Give the position of every Plasmodium parasite.
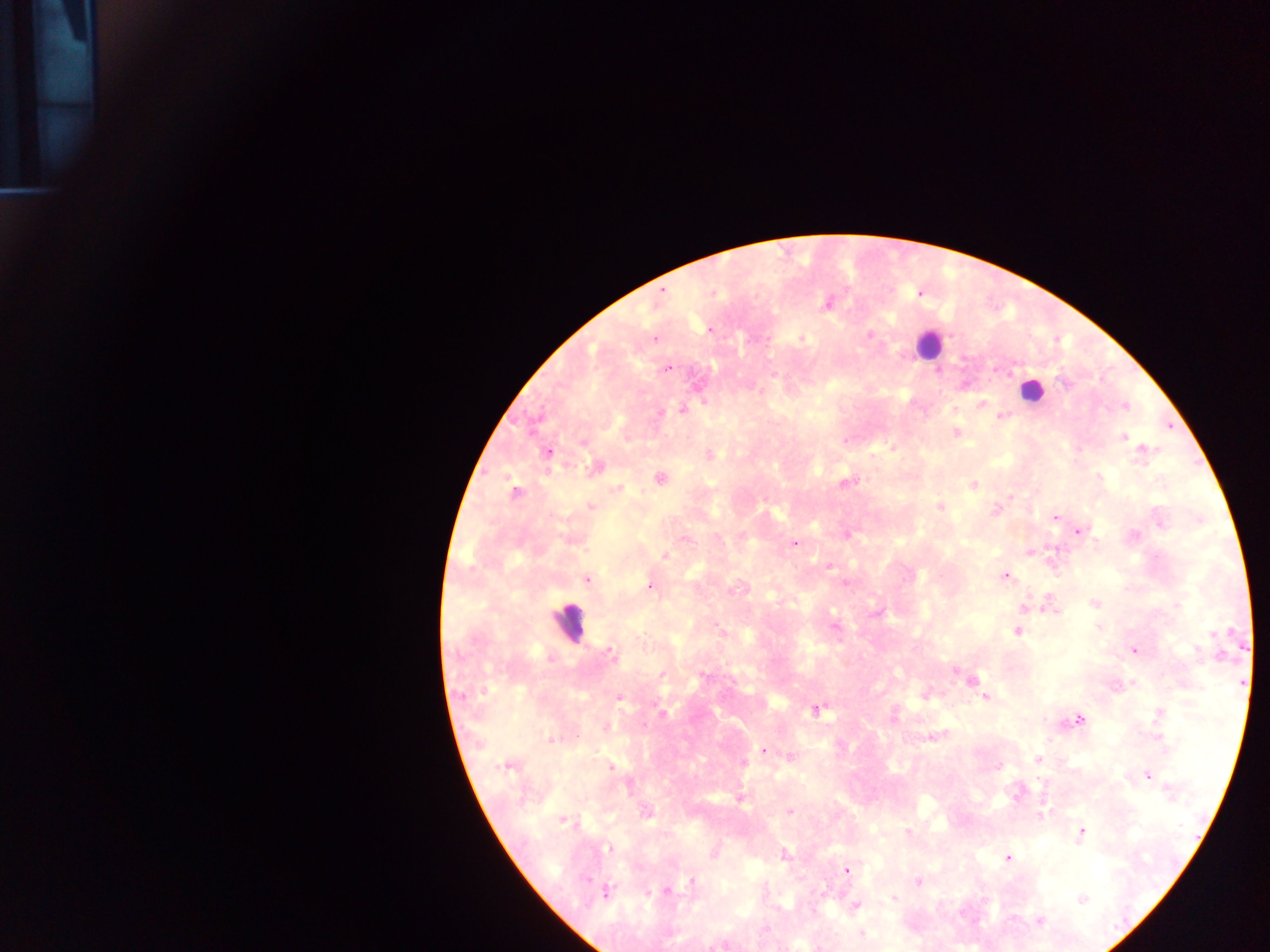
Approximate centers as {x, y} in pixels.
Plasmodium parasites: {663, 291}, {713, 293}, {919, 293}, {827, 303}, {709, 331}, {870, 334}, {654, 339}, {800, 339}, {666, 370}, {774, 374}, {1066, 384}, {982, 403}, {1125, 406}, {682, 410}, {660, 412}, {1000, 416}, {956, 432}, {1124, 437}, {583, 443}, {893, 447}, {548, 452}, {1145, 452}, {710, 454}, {594, 468}, {1099, 477}, {661, 479}, {847, 483}, {973, 485}, {617, 489}, {514, 493}, {1010, 497}, {591, 507}, {939, 507}, {995, 510}, {1055, 517}, {1080, 531}, {1134, 534}, {846, 535}, {687, 539}, {795, 543}, {1030, 551}, {665, 555}, {830, 565}, {1006, 576}, {587, 579}, {845, 582}, {650, 587}, {740, 588}, {1094, 604}, {1025, 606}, {1052, 609}, {877, 612}, {835, 627}, {1099, 627}, {721, 631}, {1017, 632}, {1134, 651}, {610, 652}, {550, 657}, {956, 670}, {662, 675}, {704, 676}, {971, 681}, {975, 686}, {462, 696}, {926, 696}, {620, 698}, {986, 698}, {816, 710}, {662, 711}, {1158, 714}, {1079, 720}, {606, 727}, {936, 736}, {551, 738}, {1050, 739}, {763, 751}, {790, 756}, {1039, 759}, {743, 763}, {505, 767}, {611, 767}, {999, 767}, {1147, 776}, {1041, 782}, {1171, 794}, {740, 799}, {790, 811}, {1042, 814}, {646, 815}, {566, 821}, {907, 833}, {1082, 833}, {609, 848}, {785, 854}, {1007, 858}, {847, 870}, {693, 881}, {918, 881}, {666, 891}, {606, 893}, {648, 893}, {895, 898}, {1083, 899}, {856, 906}, {1012, 918}, {1040, 921}, {766, 929}, {863, 933}.

Leukocyte locations: {929, 344}, {1030, 391}, {570, 624}. One field of view. Sample from Ghana. Thick blood film. Mobile-phone photograph taken through the microscope. Image is 1270×952 pixels.